Identify the cell.
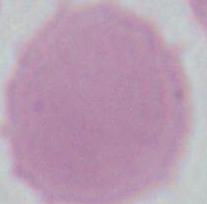

An erythrocyte.

{
  "magnification": "1000x",
  "modality": "micrograph"
}